Assess this cell for malaria.
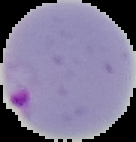
Parasitized.

Summary:
  - Image type: cell region segmented out of the field of view; surrounding area masked to black
  - Preparation: thin blood smear
  - Image size: 136×142 pixels